Find each WBC.
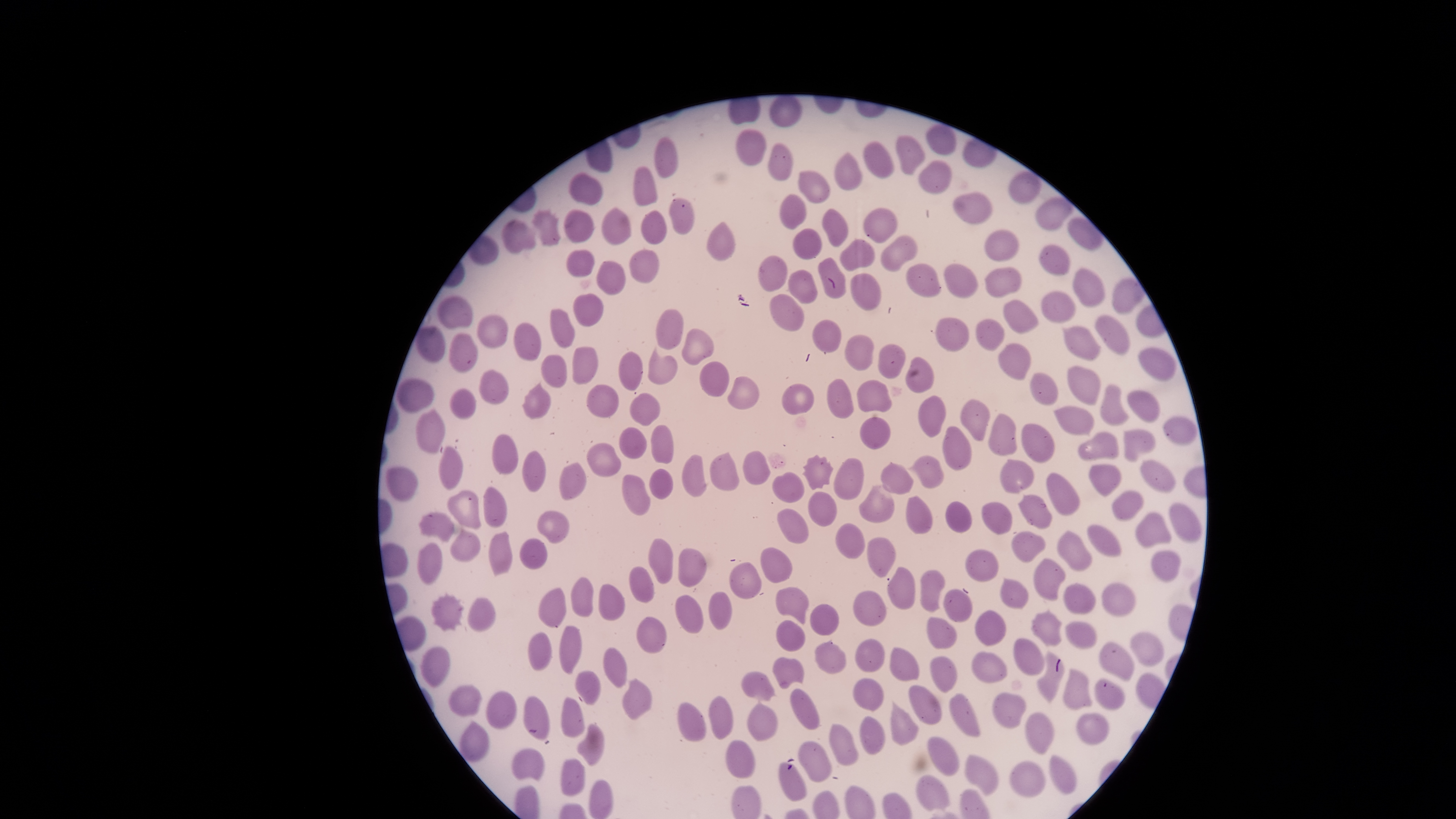
No WBCs identified.

Approximate bounding boxes, in pixels from the top-left corner.
Summary:
  - Uninfected RBCs: (left=769, top=96, right=801, bottom=126), (left=925, top=123, right=956, bottom=154), (left=735, top=128, right=766, bottom=165), (left=895, top=135, right=926, bottom=174), (left=653, top=136, right=678, bottom=178), (left=864, top=140, right=894, bottom=179), (left=767, top=142, right=793, bottom=181), (left=834, top=152, right=863, bottom=191), (left=920, top=160, right=952, bottom=193), (left=634, top=166, right=658, bottom=206), (left=798, top=170, right=831, bottom=204), (left=569, top=172, right=604, bottom=205), (left=1007, top=172, right=1042, bottom=204), (left=952, top=191, right=993, bottom=224), (left=779, top=193, right=806, bottom=229), (left=669, top=197, right=696, bottom=234), (left=531, top=207, right=559, bottom=246), (left=602, top=207, right=631, bottom=244), (left=822, top=208, right=848, bottom=246), (left=862, top=208, right=898, bottom=243), (left=564, top=209, right=594, bottom=242), (left=638, top=211, right=666, bottom=244), (left=502, top=220, right=535, bottom=255), (left=707, top=220, right=736, bottom=263), (left=791, top=228, right=821, bottom=260), (left=985, top=228, right=1019, bottom=261), (left=880, top=235, right=917, bottom=271), (left=839, top=239, right=875, bottom=272), (left=1039, top=244, right=1069, bottom=276), (left=567, top=249, right=594, bottom=277), (left=629, top=250, right=659, bottom=283), (left=758, top=255, right=788, bottom=291), (left=818, top=257, right=847, bottom=299), (left=596, top=261, right=626, bottom=296), (left=943, top=263, right=977, bottom=298), (left=906, top=264, right=940, bottom=297), (left=986, top=267, right=1022, bottom=298), (left=1072, top=268, right=1104, bottom=308), (left=787, top=270, right=817, bottom=304), (left=850, top=273, right=881, bottom=311), (left=1110, top=277, right=1145, bottom=313), (left=1040, top=289, right=1076, bottom=323), (left=573, top=294, right=604, bottom=326), (left=768, top=294, right=804, bottom=332), (left=436, top=296, right=473, bottom=329), (left=1003, top=300, right=1040, bottom=335), (left=549, top=309, right=577, bottom=347), (left=655, top=309, right=684, bottom=349), (left=478, top=314, right=508, bottom=350), (left=1095, top=314, right=1129, bottom=356), (left=935, top=317, right=968, bottom=352), (left=811, top=319, right=841, bottom=352), (left=976, top=319, right=1003, bottom=351), (left=513, top=321, right=542, bottom=361), (left=1062, top=325, right=1101, bottom=360), (left=416, top=326, right=445, bottom=364), (left=681, top=328, right=714, bottom=364), (left=450, top=332, right=478, bottom=373), (left=844, top=335, right=874, bottom=371), (left=997, top=343, right=1031, bottom=381), (left=877, top=344, right=905, bottom=379), (left=572, top=347, right=599, bottom=385), (left=1137, top=348, right=1175, bottom=381), (left=618, top=350, right=642, bottom=391), (left=541, top=354, right=567, bottom=388), (left=905, top=357, right=935, bottom=393), (left=700, top=360, right=729, bottom=397), (left=1067, top=365, right=1100, bottom=405), (left=480, top=369, right=508, bottom=405), (left=1030, top=373, right=1059, bottom=406), (left=728, top=376, right=760, bottom=409), (left=397, top=378, right=434, bottom=412), (left=827, top=379, right=854, bottom=419), (left=522, top=380, right=550, bottom=418), (left=856, top=380, right=892, bottom=413), (left=1100, top=384, right=1129, bottom=426), (left=586, top=385, right=619, bottom=417), (left=781, top=385, right=814, bottom=415), (left=449, top=388, right=475, bottom=420), (left=1127, top=390, right=1160, bottom=422), (left=630, top=393, right=661, bottom=426), (left=918, top=395, right=946, bottom=438), (left=960, top=400, right=989, bottom=441), (left=416, top=407, right=445, bottom=453), (left=1054, top=408, right=1094, bottom=435), (left=988, top=414, right=1016, bottom=455), (left=1164, top=416, right=1198, bottom=446), (left=858, top=417, right=891, bottom=450), (left=1021, top=424, right=1055, bottom=464), (left=651, top=425, right=673, bottom=464), (left=943, top=426, right=971, bottom=471), (left=618, top=427, right=646, bottom=458), (left=1124, top=430, right=1156, bottom=462), (left=1078, top=432, right=1119, bottom=460), (left=492, top=433, right=518, bottom=474), (left=586, top=442, right=621, bottom=477), (left=438, top=447, right=462, bottom=489), (left=522, top=450, right=546, bottom=493), (left=742, top=451, right=770, bottom=486), (left=709, top=453, right=739, bottom=491), (left=682, top=454, right=707, bottom=497), (left=801, top=454, right=835, bottom=490), (left=906, top=455, right=944, bottom=490), (left=833, top=458, right=864, bottom=500), (left=1000, top=460, right=1034, bottom=494), (left=1140, top=460, right=1175, bottom=493), (left=559, top=461, right=586, bottom=501), (left=882, top=464, right=914, bottom=494), (left=1089, top=465, right=1122, bottom=497), (left=385, top=466, right=419, bottom=502), (left=650, top=469, right=672, bottom=499), (left=771, top=472, right=803, bottom=502), (left=1046, top=473, right=1081, bottom=515), (left=623, top=474, right=650, bottom=516), (left=483, top=486, right=507, bottom=526), (left=859, top=486, right=895, bottom=522), (left=1112, top=489, right=1144, bottom=521), (left=447, top=491, right=481, bottom=529), (left=808, top=491, right=836, bottom=526), (left=907, top=494, right=933, bottom=533), (left=1018, top=495, right=1051, bottom=528), (left=945, top=500, right=972, bottom=533), (left=982, top=501, right=1012, bottom=534), (left=1168, top=502, right=1202, bottom=542), (left=776, top=508, right=809, bottom=544), (left=536, top=509, right=570, bottom=543), (left=419, top=512, right=454, bottom=542), (left=1133, top=513, right=1171, bottom=548), (left=834, top=522, right=864, bottom=559), (left=1088, top=525, right=1122, bottom=557), (left=449, top=528, right=481, bottom=561), (left=1057, top=530, right=1092, bottom=571), (left=489, top=531, right=513, bottom=576), (left=1012, top=532, right=1046, bottom=563), (left=866, top=536, right=896, bottom=578), (left=519, top=537, right=548, bottom=570), (left=648, top=539, right=672, bottom=585), (left=417, top=542, right=443, bottom=583), (left=760, top=546, right=793, bottom=584), (left=679, top=548, right=706, bottom=587), (left=965, top=548, right=1000, bottom=583), (left=1151, top=551, right=1181, bottom=583), (left=1033, top=559, right=1065, bottom=601), (left=728, top=562, right=762, bottom=599), (left=629, top=566, right=655, bottom=604), (left=887, top=567, right=914, bottom=611), (left=920, top=569, right=945, bottom=613), (left=570, top=576, right=594, bottom=617), (left=1000, top=578, right=1028, bottom=608), (left=597, top=583, right=625, bottom=621), (left=1101, top=583, right=1135, bottom=616), (left=1063, top=584, right=1095, bottom=613), (left=775, top=586, right=809, bottom=623), (left=538, top=587, right=565, bottom=628), (left=943, top=589, right=973, bottom=622), (left=708, top=590, right=733, bottom=631), (left=852, top=590, right=887, bottom=626), (left=432, top=591, right=463, bottom=633), (left=674, top=594, right=703, bottom=634), (left=468, top=596, right=497, bottom=634), (left=810, top=604, right=839, bottom=635), (left=976, top=610, right=1006, bottom=645), (left=1031, top=610, right=1062, bottom=646), (left=636, top=617, right=666, bottom=653), (left=926, top=617, right=958, bottom=649), (left=776, top=620, right=806, bottom=652), (left=1065, top=621, right=1096, bottom=648), (left=558, top=626, right=582, bottom=673), (left=527, top=632, right=553, bottom=670), (left=1129, top=632, right=1163, bottom=667), (left=814, top=638, right=845, bottom=675), (left=855, top=638, right=885, bottom=672), (left=1013, top=638, right=1044, bottom=675), (left=1098, top=643, right=1133, bottom=681), (left=422, top=646, right=451, bottom=688), (left=890, top=646, right=919, bottom=681), (left=602, top=647, right=627, bottom=688), (left=1036, top=651, right=1063, bottom=703), (left=971, top=652, right=1007, bottom=683), (left=773, top=656, right=803, bottom=688), (left=930, top=656, right=957, bottom=693), (left=574, top=669, right=599, bottom=704), (left=1063, top=669, right=1092, bottom=711), (left=741, top=672, right=774, bottom=700), (left=621, top=677, right=652, bottom=720), (left=853, top=678, right=885, bottom=710), (left=1095, top=679, right=1124, bottom=709), (left=449, top=685, right=482, bottom=717), (left=909, top=685, right=942, bottom=726), (left=790, top=687, right=820, bottom=729), (left=486, top=691, right=516, bottom=729), (left=992, top=692, right=1027, bottom=729), (left=949, top=694, right=979, bottom=737), (left=524, top=696, right=549, bottom=738), (left=561, top=696, right=585, bottom=739), (left=708, top=696, right=733, bottom=739), (left=747, top=700, right=777, bottom=741), (left=679, top=702, right=705, bottom=742), (left=891, top=702, right=919, bottom=746), (left=1025, top=713, right=1055, bottom=754), (left=1075, top=713, right=1110, bottom=745), (left=860, top=716, right=885, bottom=754), (left=459, top=720, right=489, bottom=763), (left=576, top=723, right=604, bottom=766), (left=828, top=724, right=858, bottom=766), (left=926, top=735, right=958, bottom=775), (left=725, top=739, right=755, bottom=777), (left=798, top=741, right=833, bottom=782), (left=513, top=748, right=545, bottom=780), (left=965, top=754, right=998, bottom=796), (left=1049, top=755, right=1078, bottom=795), (left=560, top=760, right=585, bottom=796), (left=1011, top=760, right=1046, bottom=797), (left=779, top=762, right=807, bottom=801), (left=915, top=774, right=949, bottom=810), (left=588, top=779, right=613, bottom=818)
  - Field of view: single
  - Visible region: circular
  - Image size: 1456×819 pixels
  - Presence: no malaria parasites identified
  - Preparation: thin smear of blood
  - Capture: smartphone photograph through the microscope eyepiece
  - Stain: Giemsa